Name the parasite shown.
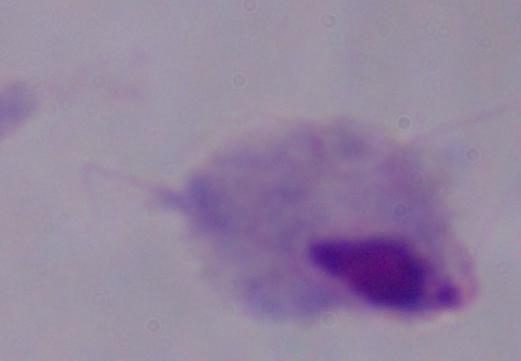
This is a trichomonad.

Summary:
  - Modality: micrograph
  - Magnification: 1000x